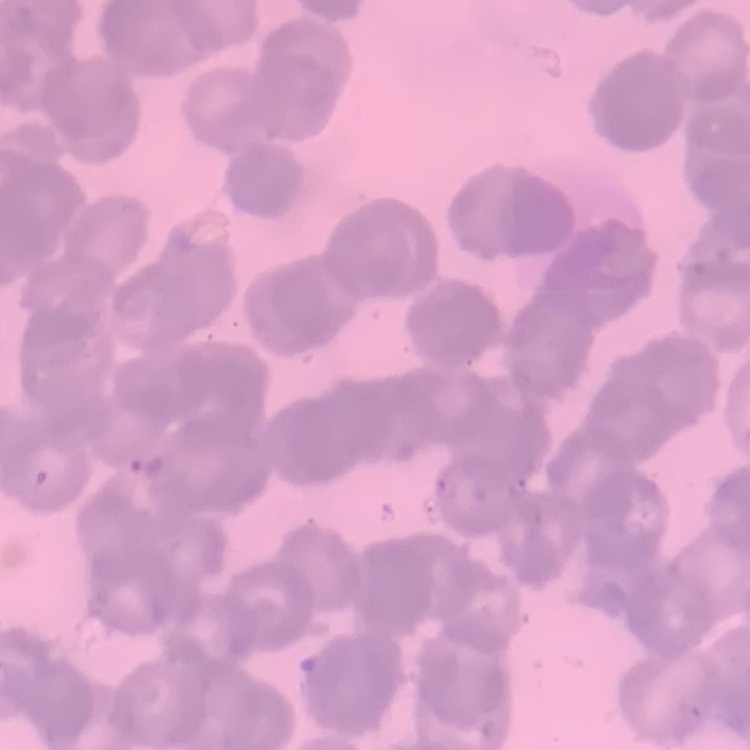

Summary:
  - Red blood cell morphology: rouleaux formation
  - Stain: Field's or Giemsa
  - Image type: one tile cut from a larger photomicrograph
  - Preparation: thin blood smear